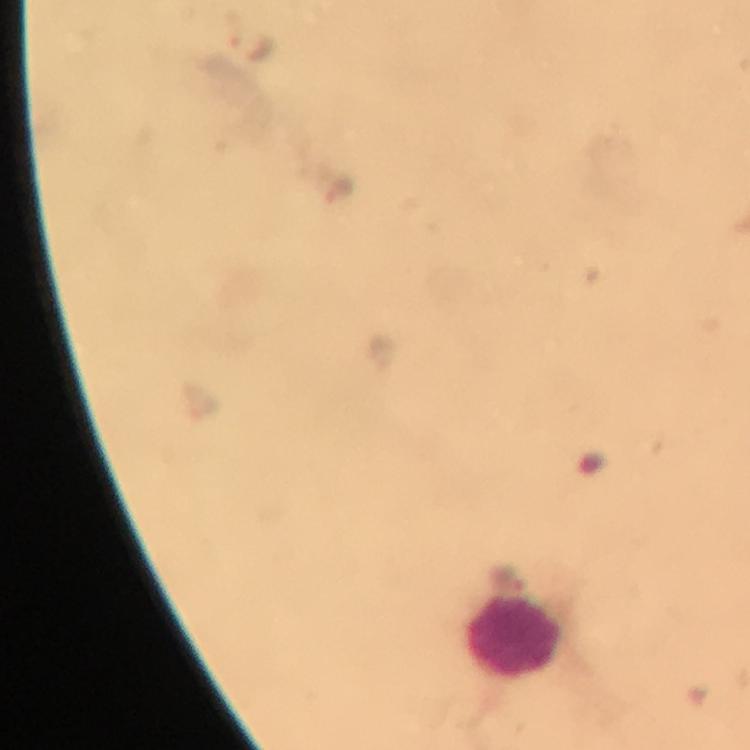

Approximate centers as (x, y) in pixels.
Summary:
  - Plasmodium parasite locations: (251, 45), (337, 187), (380, 354), (506, 579)
  - Leukocyte locations: (513, 636)
  - Immersion oil: applied
  - Preparation: thick blood smear
  - Context: from a malaria diagnostic workup
  - Magnification: 100x
  - Cropped from: one field of view
  - Stain: Giemsa
  - Capture: smartphone photograph through a microscope
  - Image size: 750×750 pixels